Report the malaria status of this cell.
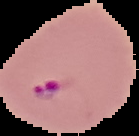
It is parasitized.

{
  "image_type": "segmented cell region with the area outside set to black",
  "image_size": "139×136 pixels",
  "preparation": "thin blood smear"
}